Outline platelets.
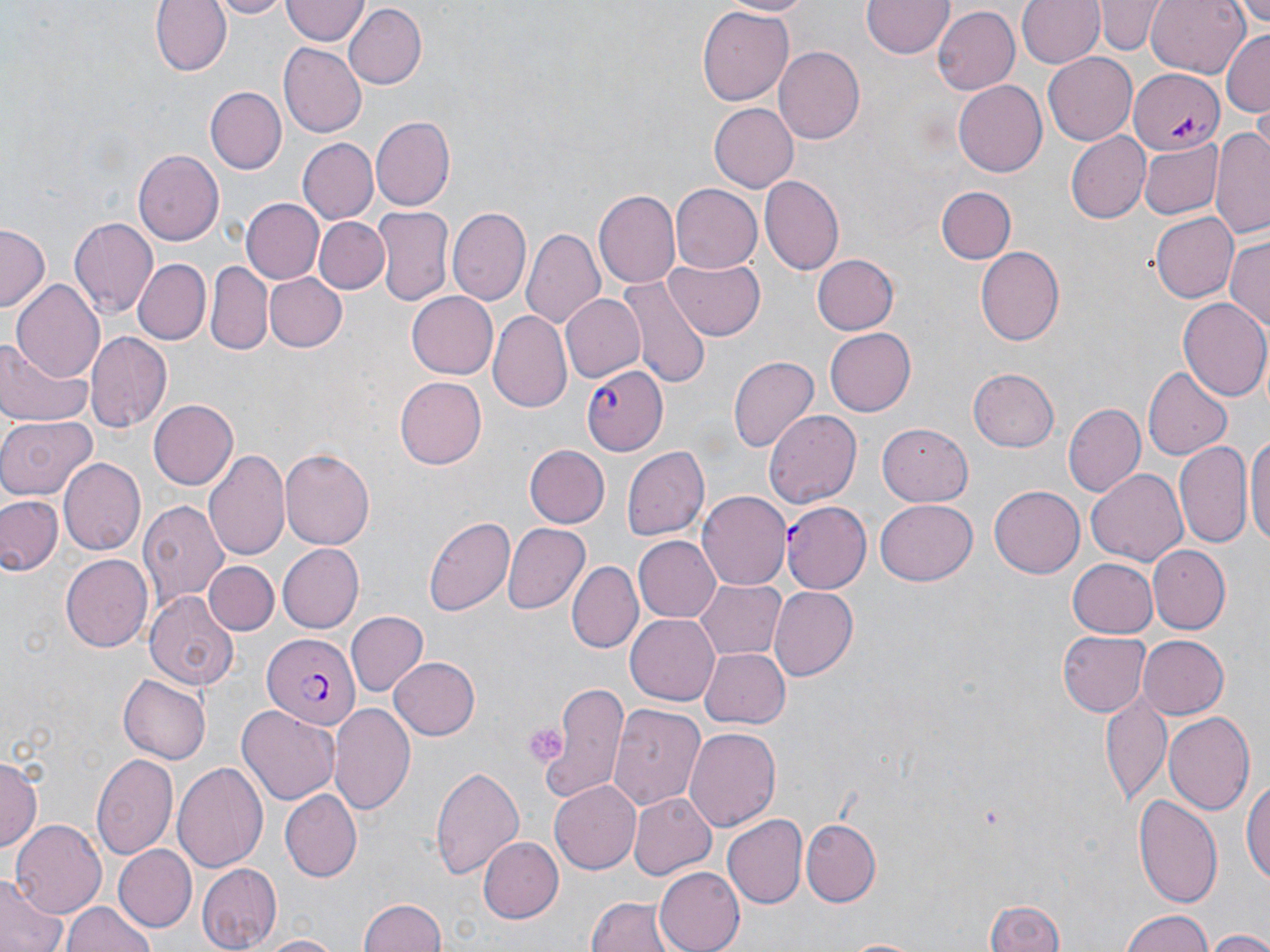
Approximate bounding boxes as named x1/y1/x2/y2 corners in pixels.
Platelets: (x1=523, y1=721, x2=565, y2=763).

Summary:
  - Plasmodium falciparum-infected red blood cell locations: (x1=1131, y1=68, x2=1224, y2=154), (x1=583, y1=364, x2=668, y2=456), (x1=781, y1=501, x2=870, y2=595), (x1=262, y1=634, x2=359, y2=730)
  - Uninfected red blood cell locations: (x1=152, y1=0, x2=229, y2=76), (x1=204, y1=0, x2=290, y2=18), (x1=718, y1=0, x2=819, y2=17), (x1=863, y1=0, x2=953, y2=60), (x1=1018, y1=0, x2=1104, y2=68), (x1=1097, y1=0, x2=1162, y2=56), (x1=1147, y1=0, x2=1250, y2=76), (x1=1227, y1=0, x2=1269, y2=39), (x1=281, y1=1, x2=368, y2=46), (x1=345, y1=4, x2=427, y2=89), (x1=697, y1=4, x2=792, y2=107), (x1=931, y1=5, x2=1020, y2=94), (x1=1222, y1=30, x2=1270, y2=119), (x1=279, y1=43, x2=366, y2=138), (x1=773, y1=46, x2=864, y2=144), (x1=1044, y1=54, x2=1137, y2=144), (x1=953, y1=81, x2=1047, y2=178), (x1=204, y1=87, x2=287, y2=175), (x1=708, y1=103, x2=798, y2=192), (x1=370, y1=115, x2=454, y2=211), (x1=1210, y1=126, x2=1270, y2=238), (x1=1066, y1=133, x2=1149, y2=223), (x1=298, y1=139, x2=378, y2=226), (x1=1139, y1=140, x2=1223, y2=220), (x1=135, y1=149, x2=225, y2=246), (x1=760, y1=175, x2=844, y2=275), (x1=672, y1=183, x2=763, y2=275), (x1=935, y1=186, x2=1015, y2=264), (x1=596, y1=189, x2=679, y2=288), (x1=242, y1=199, x2=322, y2=283), (x1=375, y1=206, x2=453, y2=306), (x1=449, y1=208, x2=531, y2=306), (x1=1151, y1=211, x2=1239, y2=302), (x1=69, y1=216, x2=157, y2=316), (x1=315, y1=218, x2=387, y2=294), (x1=0, y1=224, x2=49, y2=312), (x1=521, y1=228, x2=605, y2=331), (x1=1227, y1=234, x2=1270, y2=336), (x1=976, y1=246, x2=1065, y2=347), (x1=810, y1=254, x2=900, y2=336), (x1=131, y1=257, x2=210, y2=345), (x1=664, y1=257, x2=766, y2=340), (x1=208, y1=261, x2=274, y2=356), (x1=264, y1=272, x2=347, y2=354), (x1=616, y1=272, x2=712, y2=390), (x1=11, y1=281, x2=104, y2=383), (x1=407, y1=291, x2=499, y2=378), (x1=559, y1=292, x2=645, y2=383), (x1=1178, y1=299, x2=1270, y2=401), (x1=489, y1=311, x2=572, y2=413), (x1=824, y1=326, x2=915, y2=417), (x1=85, y1=331, x2=170, y2=431), (x1=0, y1=336, x2=94, y2=429), (x1=728, y1=355, x2=819, y2=454), (x1=968, y1=367, x2=1060, y2=452), (x1=1144, y1=367, x2=1232, y2=460), (x1=395, y1=377, x2=487, y2=468), (x1=149, y1=399, x2=238, y2=489), (x1=1062, y1=403, x2=1146, y2=497), (x1=765, y1=410, x2=863, y2=506), (x1=0, y1=415, x2=98, y2=499), (x1=878, y1=422, x2=972, y2=505), (x1=1248, y1=427, x2=1270, y2=554), (x1=1174, y1=440, x2=1252, y2=550), (x1=523, y1=444, x2=609, y2=529), (x1=621, y1=445, x2=710, y2=543), (x1=204, y1=448, x2=290, y2=565), (x1=279, y1=449, x2=373, y2=551), (x1=58, y1=457, x2=144, y2=556), (x1=1086, y1=468, x2=1188, y2=566), (x1=990, y1=485, x2=1084, y2=578), (x1=698, y1=492, x2=790, y2=590), (x1=0, y1=493, x2=62, y2=576), (x1=138, y1=496, x2=228, y2=608), (x1=875, y1=498, x2=978, y2=587), (x1=424, y1=513, x2=515, y2=616), (x1=502, y1=523, x2=590, y2=615), (x1=632, y1=536, x2=720, y2=623), (x1=279, y1=544, x2=364, y2=632), (x1=1148, y1=546, x2=1229, y2=633), (x1=59, y1=553, x2=150, y2=651), (x1=1067, y1=557, x2=1160, y2=638), (x1=205, y1=560, x2=278, y2=636), (x1=568, y1=562, x2=639, y2=652), (x1=694, y1=579, x2=785, y2=659), (x1=769, y1=586, x2=859, y2=679), (x1=144, y1=591, x2=241, y2=689), (x1=345, y1=612, x2=427, y2=697), (x1=625, y1=614, x2=719, y2=705), (x1=1057, y1=629, x2=1149, y2=718), (x1=1136, y1=634, x2=1229, y2=718), (x1=701, y1=645, x2=790, y2=729), (x1=389, y1=656, x2=481, y2=741), (x1=118, y1=674, x2=210, y2=764), (x1=545, y1=683, x2=631, y2=800), (x1=1101, y1=693, x2=1172, y2=806), (x1=609, y1=703, x2=704, y2=809), (x1=235, y1=704, x2=340, y2=805), (x1=329, y1=704, x2=416, y2=816), (x1=1163, y1=712, x2=1256, y2=814), (x1=683, y1=728, x2=782, y2=833), (x1=91, y1=751, x2=178, y2=862), (x1=0, y1=755, x2=40, y2=853), (x1=172, y1=761, x2=271, y2=873), (x1=431, y1=765, x2=523, y2=881), (x1=1242, y1=773, x2=1269, y2=890), (x1=549, y1=779, x2=640, y2=873), (x1=282, y1=789, x2=361, y2=880), (x1=628, y1=792, x2=717, y2=881), (x1=1133, y1=793, x2=1223, y2=906), (x1=724, y1=815, x2=807, y2=908), (x1=800, y1=818, x2=880, y2=907), (x1=11, y1=821, x2=105, y2=920), (x1=477, y1=836, x2=563, y2=922), (x1=112, y1=845, x2=195, y2=932), (x1=197, y1=863, x2=282, y2=950), (x1=655, y1=865, x2=750, y2=952), (x1=0, y1=875, x2=65, y2=952), (x1=584, y1=895, x2=678, y2=952), (x1=987, y1=897, x2=1067, y2=952), (x1=358, y1=898, x2=448, y2=952), (x1=64, y1=903, x2=153, y2=952), (x1=1118, y1=909, x2=1217, y2=951), (x1=1205, y1=930, x2=1270, y2=952), (x1=254, y1=935, x2=343, y2=952)
  - Slide-level diagnosis: Plasmodium falciparum
  - Magnification: 1000x
  - Image size: 1270×952 pixels
  - Modality: light microscopy
  - Field of view: single
  - Preparation: thin blood smear
  - Stain: May-Grünwald-Giemsa